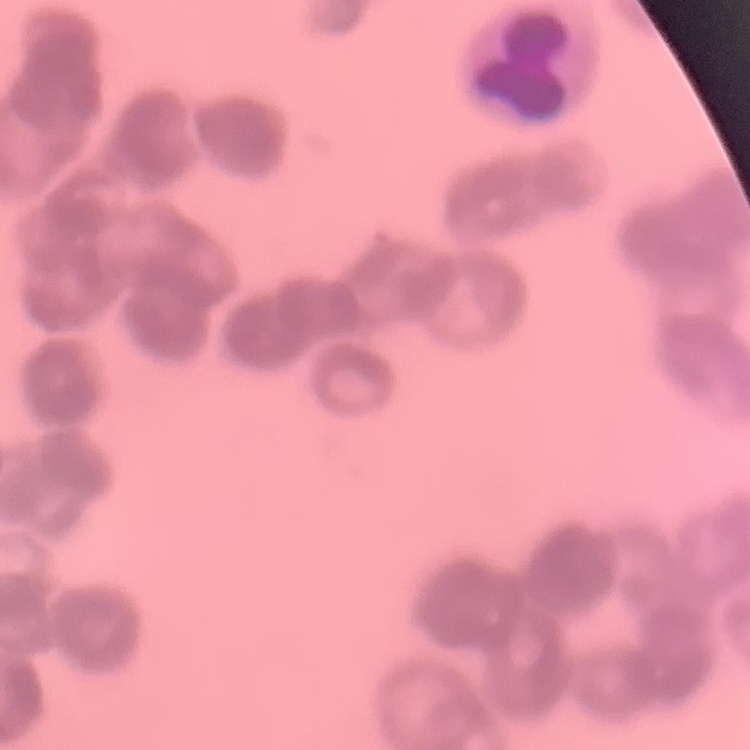
Summary:
  - Erythrocyte morphology: rouleaux formation
  - Image type: one tile cut from a larger photomicrograph
  - Stain: Field's or Giemsa
  - Preparation: thin blood smear